Name the parasite shown.
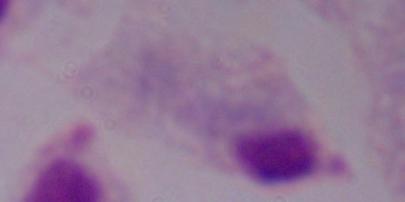

This is a trichomonad.

{
  "modality": "micrograph",
  "magnification": "1000x"
}